Classify this cell by malaria status.
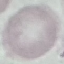

It is uninfected.

Summary:
  - Stain: Giemsa
  - Preparation: thin blood smear
  - Capture: smartphone camera at the microscope eyepiece
  - Image type: cell patch, automatically extracted from a larger field of view and resized to 64 × 64 pixels